Comment on the morphology of the erythrocytes.
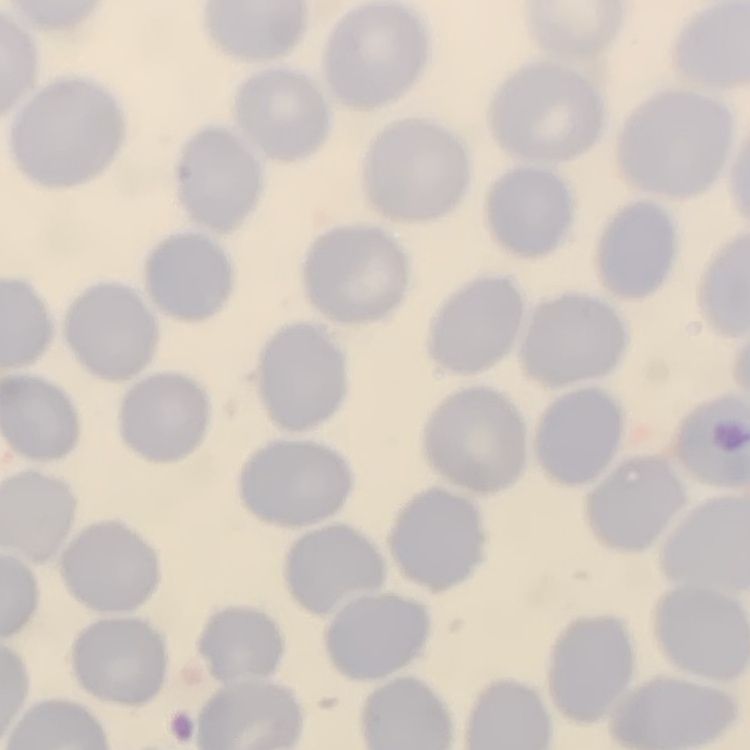

They show no rouleaux formation.

{
  "stain": "Field's or Giemsa",
  "image_type": "one tile cut from a larger photomicrograph",
  "preparation": "thin blood film"
}